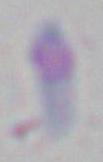
magnification = 1000x
identification = Toxoplasma gondii
modality = micrograph